Name the cell type shown.
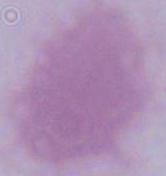

An erythrocyte.

modality = photomicrograph
magnification = 1000x